Locate every uninfected red blood cell.
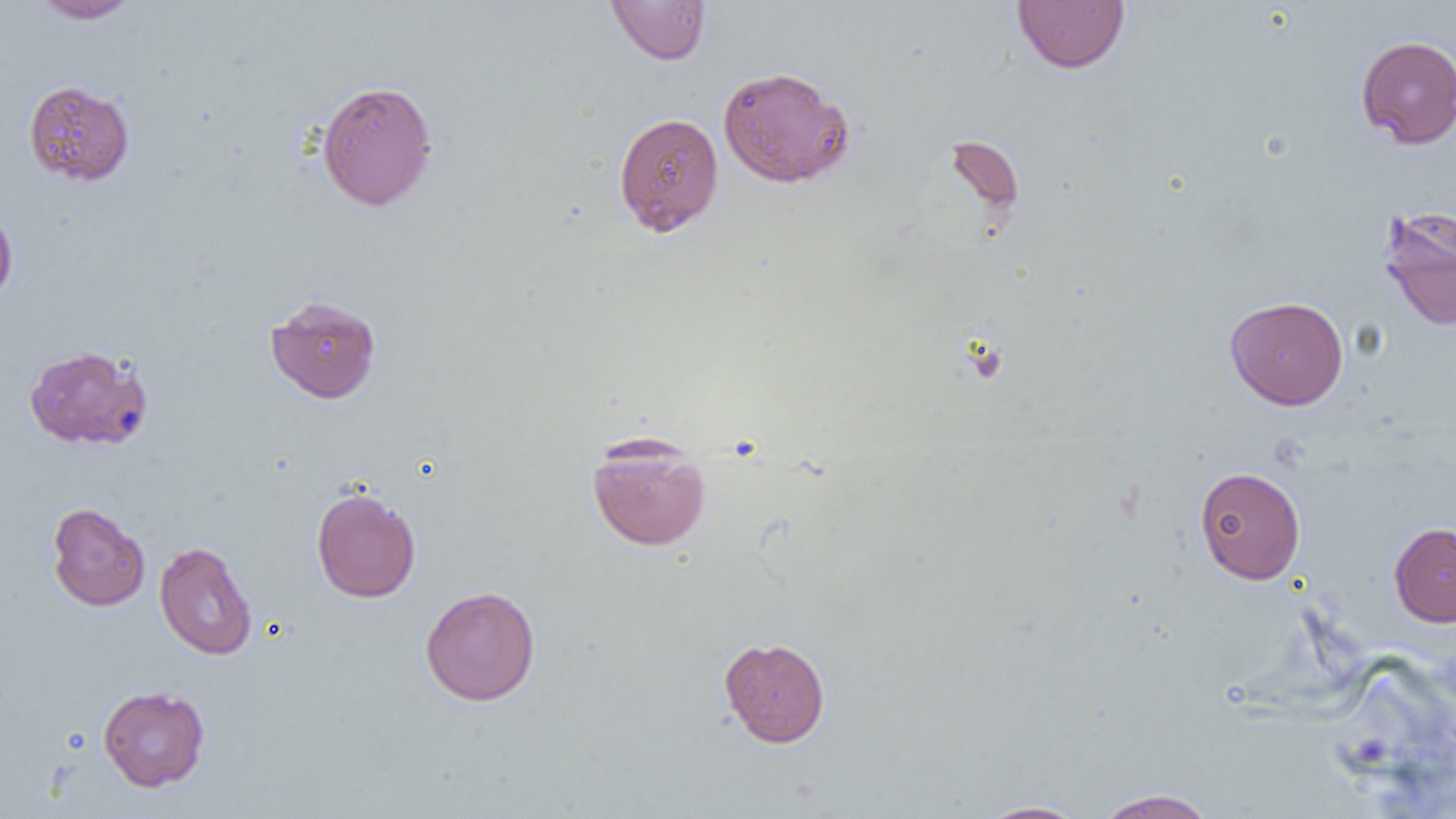
Approximate bounding boxes as (x1, y1, x2, y2) in pixels.
Uninfected red blood cells: (30, 0, 140, 23), (605, 0, 711, 65), (1012, 1, 1130, 73), (1356, 35, 1456, 148), (717, 65, 855, 189), (23, 79, 135, 185), (316, 79, 438, 211), (613, 112, 725, 236), (945, 135, 1025, 222), (1377, 205, 1456, 332), (0, 206, 18, 308), (265, 294, 382, 404), (1224, 296, 1349, 410), (23, 344, 154, 451), (587, 436, 711, 551), (1194, 466, 1305, 584), (311, 486, 421, 602), (46, 502, 150, 611), (1389, 522, 1456, 627), (154, 540, 257, 660), (420, 586, 541, 706), (719, 637, 831, 747), (97, 685, 210, 791), (1092, 788, 1219, 818), (974, 799, 1092, 819).

slide-level diagnosis = negative for blood parasites
image size = 1456×819 pixels
preparation = thin blood smear
magnification = 1000x
field of view = one of a larger specimen
modality = optical microscopy